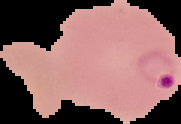

{
  "image_type": "segmented cell region on a black background",
  "result": "Plasmodium parasites identified",
  "preparation": "thin blood smear",
  "image_size": "181×124 pixels"
}